Assess this cell for malaria.
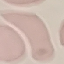

It is uninfected.

Summary:
  - Capture: smartphone through the microscope eyepiece
  - Preparation: thin smear
  - Image type: automatically extracted cell patch, resized to 64 × 64 pixels
  - Stain: Giemsa